Locate every blood parasite and identify its species.
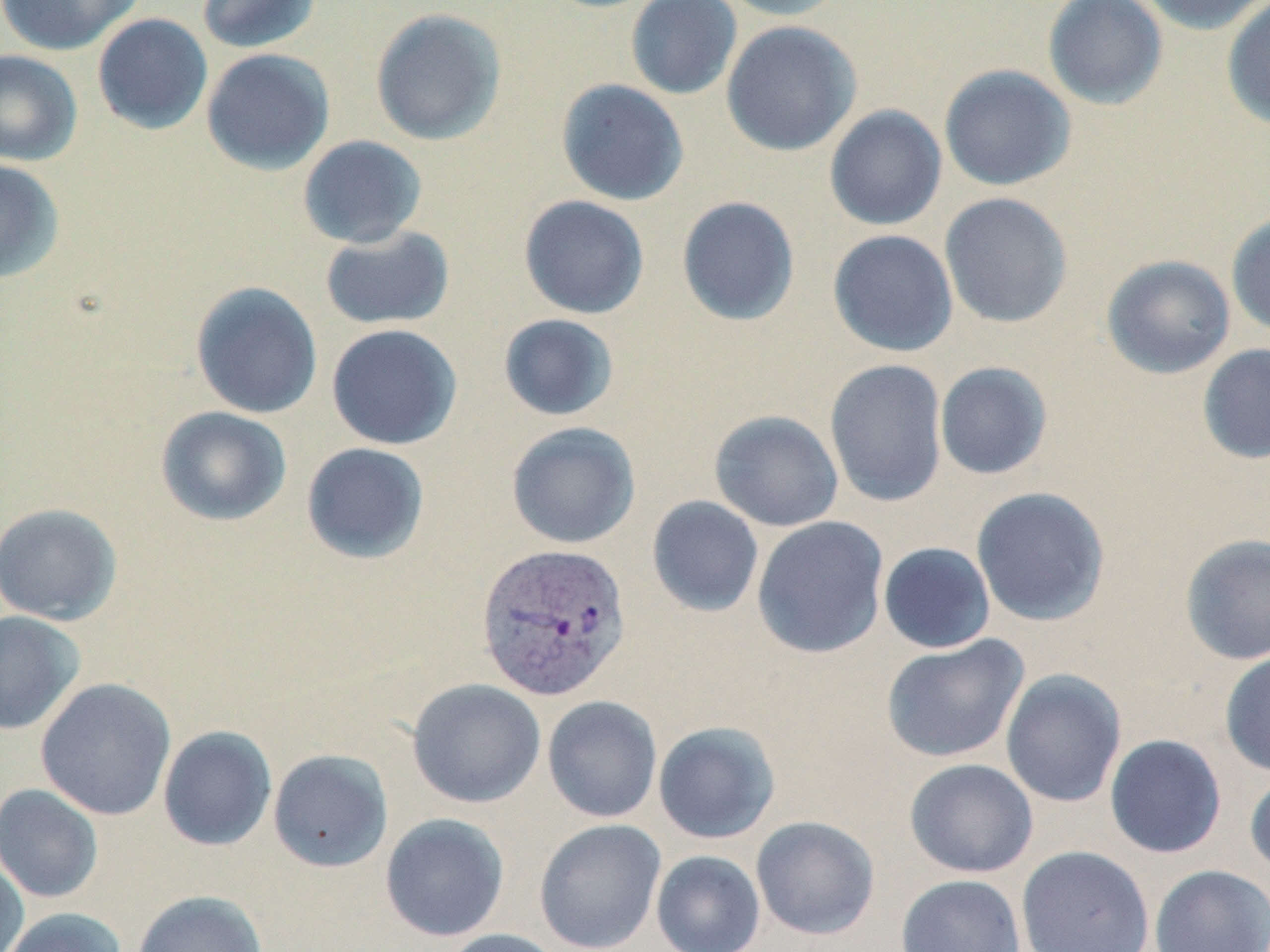
Approximate bounding boxes as [x1, y1, x2, y2] in pixels.
Plasmodium vivax-infected red blood cells: [475, 542, 633, 702].
No Plasmodium falciparum, Plasmodium ovale, Plasmodium malariae, Babesia divergens, or Trypanosoma brucei observed.

Summary:
  - Uninfected red blood cell locations: [0, 0, 145, 56], [196, 0, 322, 54], [625, 0, 742, 99], [715, 0, 850, 21], [1042, 0, 1168, 110], [1135, 0, 1270, 35], [1221, 1, 1270, 130], [370, 8, 507, 146], [92, 13, 213, 135], [721, 20, 861, 156], [201, 48, 336, 175], [0, 50, 83, 166], [939, 64, 1077, 191], [555, 79, 690, 206], [824, 105, 948, 231], [297, 135, 428, 249], [0, 159, 66, 283], [939, 192, 1074, 328], [518, 195, 650, 319], [676, 196, 800, 326], [1226, 211, 1270, 339], [319, 226, 455, 330], [827, 229, 959, 357], [1101, 254, 1236, 380], [190, 281, 324, 419], [497, 313, 620, 422], [326, 323, 463, 450], [1197, 343, 1270, 465], [824, 358, 949, 507], [934, 362, 1053, 480], [156, 406, 292, 527], [709, 410, 844, 532], [506, 421, 641, 549], [301, 442, 430, 565], [970, 486, 1111, 627], [646, 495, 764, 618], [0, 502, 123, 625], [751, 516, 890, 660], [1179, 533, 1270, 665], [878, 542, 996, 654], [0, 610, 86, 735], [880, 634, 1030, 763], [1219, 648, 1270, 777], [1000, 669, 1127, 807], [35, 678, 177, 821], [407, 678, 546, 808], [542, 695, 663, 823], [653, 721, 781, 844], [157, 725, 278, 851], [1104, 734, 1227, 859], [268, 749, 393, 873], [904, 758, 1039, 878], [1245, 770, 1270, 879], [0, 783, 104, 903], [380, 813, 510, 942], [750, 815, 880, 940], [533, 819, 667, 951], [1016, 845, 1155, 952], [651, 850, 765, 952], [0, 851, 29, 952], [1150, 864, 1270, 952], [895, 874, 1027, 952], [132, 890, 267, 952], [1, 906, 128, 952], [438, 928, 569, 952]
  - Slide-level diagnosis: Plasmodium vivax
  - Magnification: 1000x
  - Stain: May-Grünwald-Giemsa
  - Field of view: single
  - Modality: optical microscopy
  - Image size: 1270×952 pixels
  - Preparation: thin blood smear